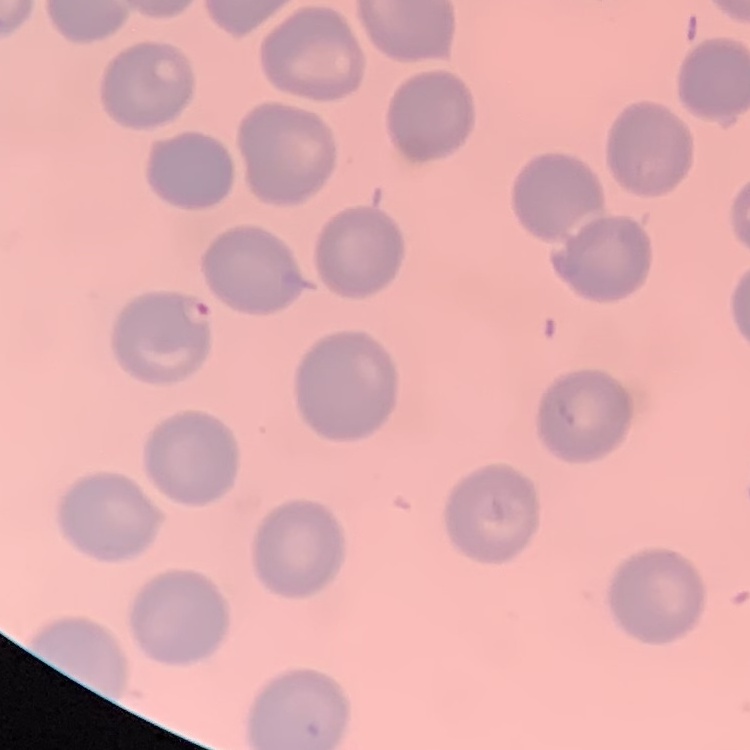

red blood cell morphology = no rouleaux formation
image type = one tile cut from a larger photomicrograph
stain = Field's or Giemsa
preparation = thin blood film